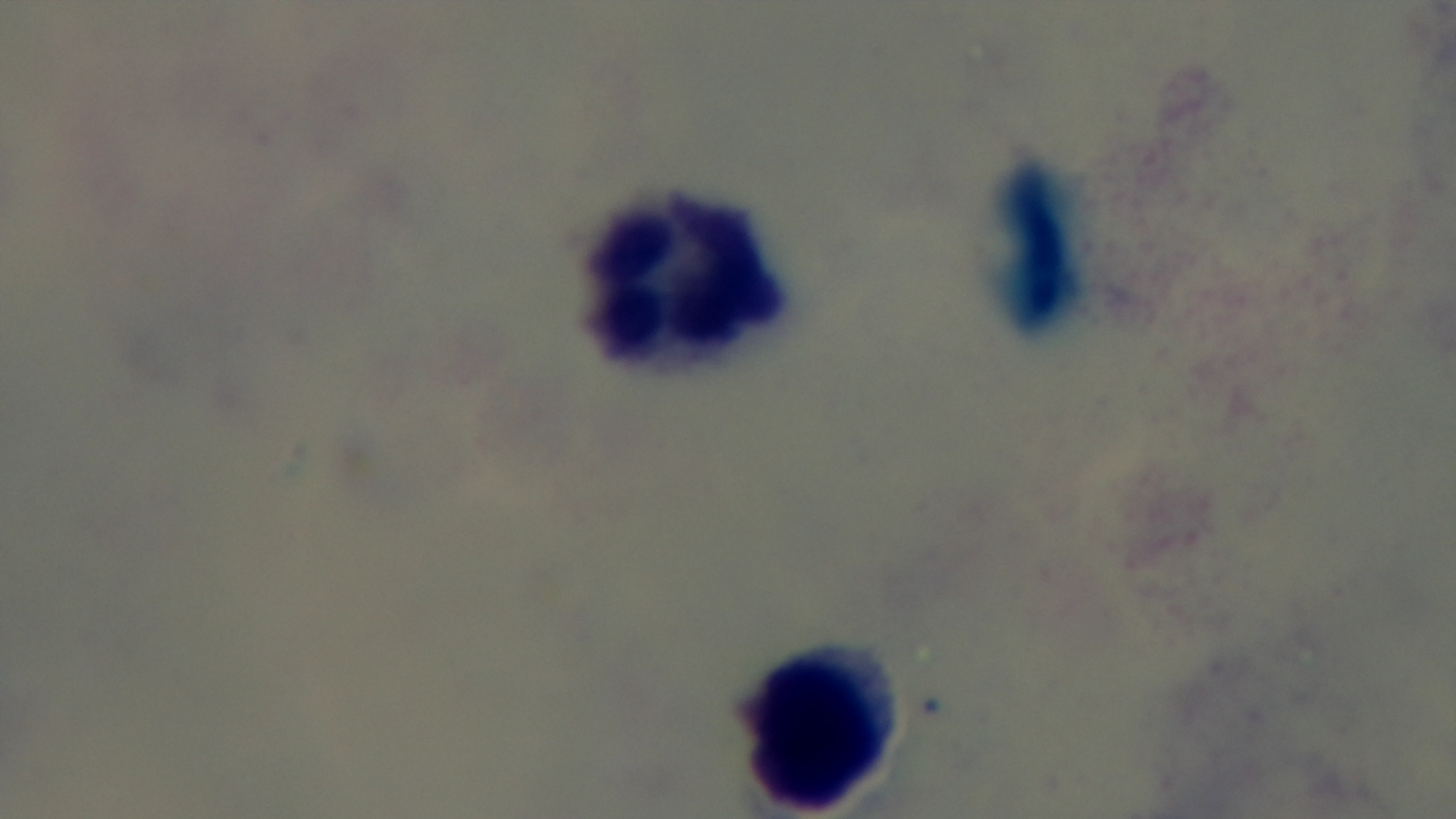

Single field of view. Preparation: thick blood film. Giemsa stain. 100x oil-immersion objective. Light microscopy. Malaria status: negative. Mounted 4K digital camera.